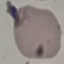

Summary:
  - Result: no malaria parasites detected
  - Stain: Giemsa
  - Image type: automatically extracted cell patch, resized to 64 × 64 pixels
  - Preparation: thin smear
  - Capture: smartphone camera at the microscope eyepiece